Name the cell type shown.
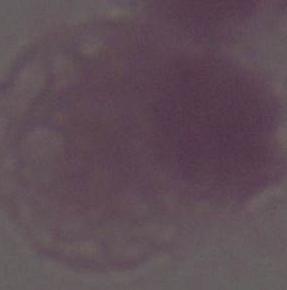

An erythrocyte.

Summary:
  - Modality: micrograph
  - Magnification: 1000x